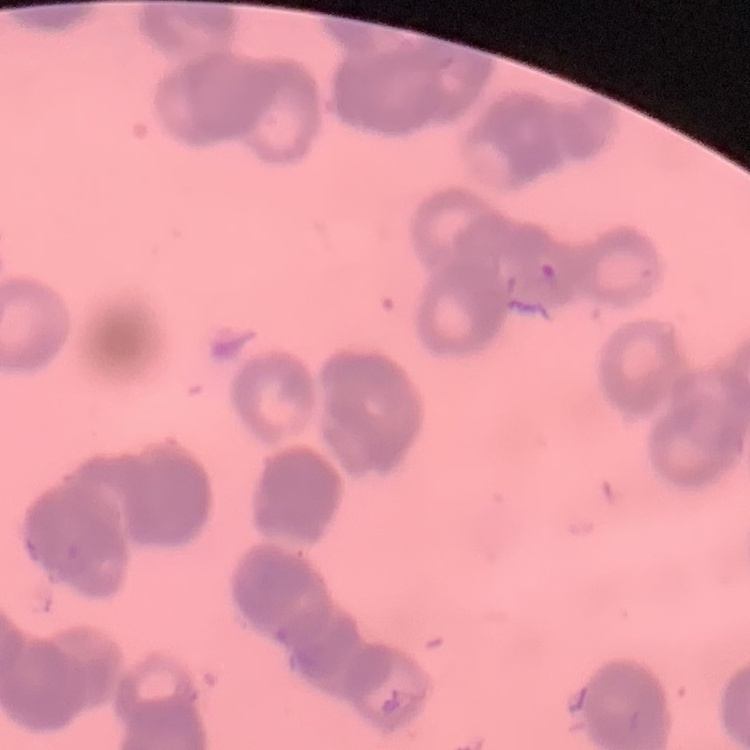

The erythrocytes exhibit rouleaux formation. Stained with either Field's or Giemsa. Square crop of a larger photomicrograph. Thin peripheral smear.